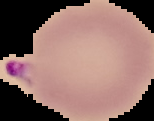
image_size: 154×121 pixels
preparation: thin blood film
image_type: segmented cell region on a black background
malaria_status: parasitized